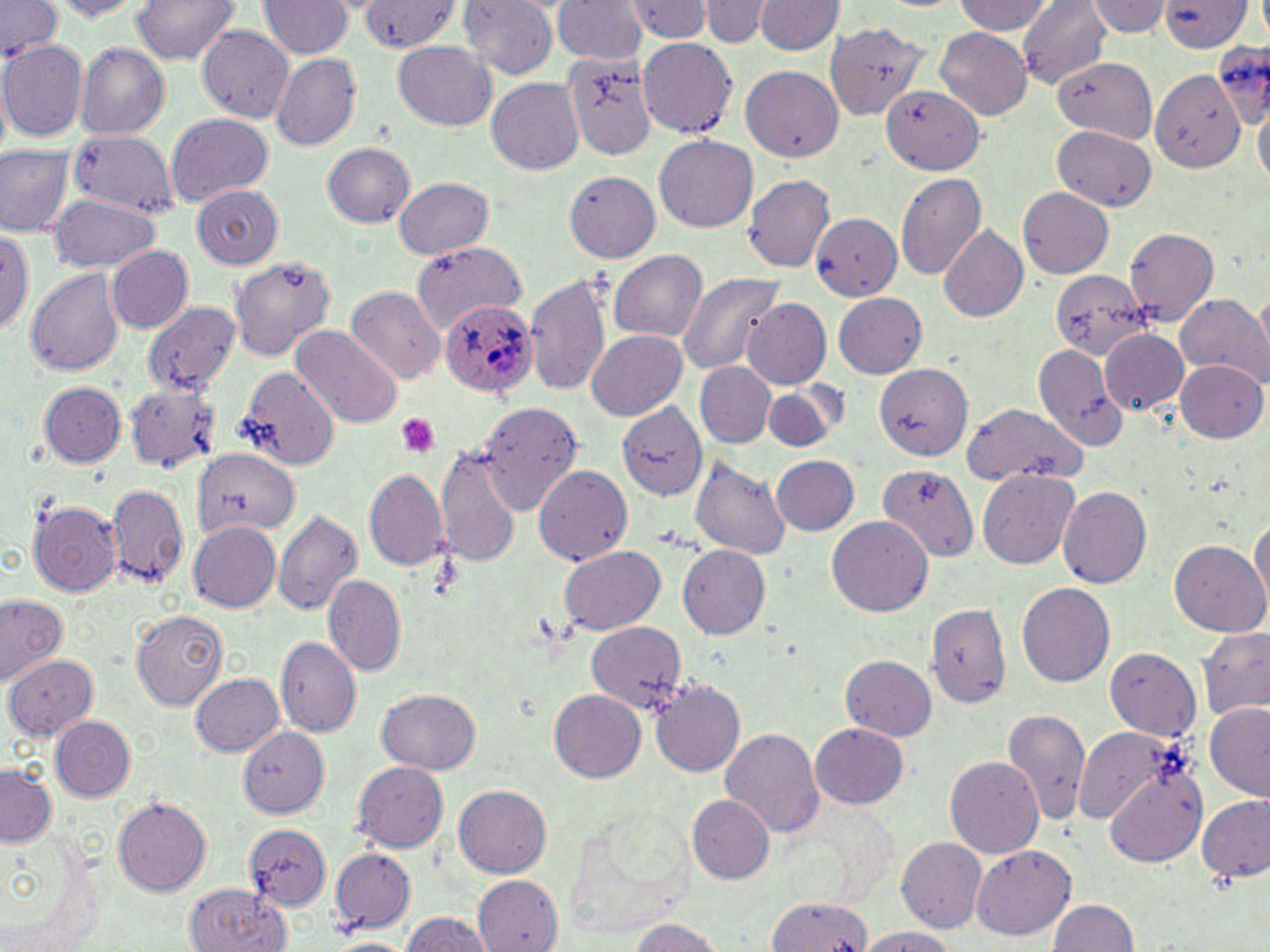
Plasmodium ovale-infected red blood cell locations = approximate bounding boxes as named x1/y1/x2/y2 corners in pixels: (x1=438, y1=297, x2=535, y2=396)
slide-level diagnosis = Plasmodium ovale
image size = 1270×952 pixels
platelet locations = approximate bounding boxes as named x1/y1/x2/y2 corners in pixels: (x1=396, y1=413, x2=439, y2=458)
field of view = one of a larger specimen
magnification = 1000x
stain = May-Grünwald-Giemsa
modality = optical microscopy
uninfected red blood cell locations = approximate bounding boxes as named x1/y1/x2/y2 corners in pixels: (x1=1, y1=0, x2=62, y2=57), (x1=129, y1=0, x2=240, y2=63), (x1=624, y1=0, x2=716, y2=44), (x1=695, y1=0, x2=777, y2=48), (x1=752, y1=0, x2=844, y2=56), (x1=1017, y1=0, x2=1111, y2=88), (x1=1086, y1=0, x2=1172, y2=37), (x1=45, y1=1, x2=154, y2=21), (x1=258, y1=1, x2=354, y2=59), (x1=359, y1=1, x2=459, y2=52), (x1=457, y1=1, x2=561, y2=78), (x1=551, y1=1, x2=648, y2=63), (x1=953, y1=1, x2=1051, y2=35), (x1=1160, y1=1, x2=1254, y2=51), (x1=823, y1=23, x2=931, y2=122), (x1=197, y1=24, x2=294, y2=121), (x1=935, y1=28, x2=1032, y2=117), (x1=636, y1=37, x2=739, y2=140), (x1=0, y1=39, x2=87, y2=141), (x1=1212, y1=39, x2=1270, y2=130), (x1=394, y1=41, x2=496, y2=131), (x1=75, y1=43, x2=169, y2=139), (x1=564, y1=51, x2=659, y2=161), (x1=270, y1=53, x2=361, y2=150), (x1=1054, y1=59, x2=1155, y2=139), (x1=742, y1=65, x2=842, y2=162), (x1=1150, y1=69, x2=1244, y2=173), (x1=486, y1=78, x2=583, y2=175), (x1=882, y1=85, x2=986, y2=175), (x1=1254, y1=101, x2=1269, y2=191), (x1=166, y1=111, x2=274, y2=205), (x1=1054, y1=128, x2=1156, y2=211), (x1=65, y1=129, x2=179, y2=219), (x1=653, y1=135, x2=757, y2=233), (x1=0, y1=144, x2=75, y2=236), (x1=322, y1=144, x2=415, y2=226), (x1=564, y1=169, x2=662, y2=261), (x1=896, y1=172, x2=987, y2=279), (x1=742, y1=174, x2=835, y2=271), (x1=393, y1=177, x2=493, y2=258), (x1=191, y1=184, x2=283, y2=269), (x1=1018, y1=186, x2=1114, y2=278), (x1=48, y1=194, x2=161, y2=272), (x1=810, y1=213, x2=902, y2=300), (x1=937, y1=224, x2=1029, y2=321), (x1=0, y1=227, x2=33, y2=335), (x1=1122, y1=227, x2=1218, y2=325), (x1=410, y1=241, x2=524, y2=329), (x1=106, y1=247, x2=193, y2=332), (x1=610, y1=249, x2=708, y2=342), (x1=229, y1=253, x2=336, y2=359), (x1=26, y1=268, x2=123, y2=377), (x1=1049, y1=269, x2=1148, y2=359), (x1=524, y1=271, x2=611, y2=396), (x1=676, y1=273, x2=783, y2=374), (x1=346, y1=285, x2=445, y2=384), (x1=1253, y1=291, x2=1270, y2=370), (x1=833, y1=293, x2=925, y2=377), (x1=1177, y1=294, x2=1269, y2=384), (x1=742, y1=298, x2=831, y2=388), (x1=142, y1=301, x2=243, y2=395), (x1=289, y1=323, x2=402, y2=428), (x1=587, y1=329, x2=687, y2=420), (x1=1101, y1=329, x2=1188, y2=413), (x1=1032, y1=343, x2=1130, y2=452), (x1=1175, y1=359, x2=1267, y2=442), (x1=695, y1=362, x2=776, y2=448), (x1=874, y1=365, x2=975, y2=460), (x1=238, y1=367, x2=339, y2=470), (x1=39, y1=381, x2=126, y2=466), (x1=121, y1=381, x2=223, y2=474), (x1=761, y1=382, x2=845, y2=453), (x1=477, y1=402, x2=582, y2=513), (x1=961, y1=402, x2=1086, y2=487), (x1=616, y1=403, x2=708, y2=502), (x1=191, y1=445, x2=299, y2=537), (x1=437, y1=447, x2=522, y2=568), (x1=771, y1=455, x2=858, y2=535), (x1=690, y1=456, x2=791, y2=559), (x1=878, y1=462, x2=981, y2=562), (x1=533, y1=465, x2=631, y2=564), (x1=976, y1=466, x2=1078, y2=568), (x1=363, y1=467, x2=450, y2=571), (x1=104, y1=482, x2=189, y2=588), (x1=1056, y1=485, x2=1151, y2=587), (x1=27, y1=500, x2=124, y2=596), (x1=272, y1=509, x2=362, y2=616), (x1=1250, y1=512, x2=1270, y2=610), (x1=827, y1=516, x2=932, y2=616), (x1=187, y1=520, x2=281, y2=612), (x1=1169, y1=540, x2=1268, y2=637), (x1=678, y1=545, x2=769, y2=638), (x1=558, y1=546, x2=667, y2=636), (x1=323, y1=574, x2=406, y2=675), (x1=1017, y1=583, x2=1115, y2=688), (x1=0, y1=592, x2=67, y2=686), (x1=926, y1=602, x2=1012, y2=710), (x1=131, y1=609, x2=229, y2=710), (x1=585, y1=621, x2=686, y2=713), (x1=1199, y1=628, x2=1270, y2=722), (x1=276, y1=635, x2=362, y2=736), (x1=1104, y1=646, x2=1202, y2=740), (x1=840, y1=654, x2=936, y2=740), (x1=5, y1=655, x2=99, y2=740), (x1=190, y1=673, x2=282, y2=755), (x1=648, y1=679, x2=746, y2=775), (x1=378, y1=689, x2=480, y2=773), (x1=550, y1=689, x2=644, y2=781), (x1=1204, y1=702, x2=1270, y2=802), (x1=1003, y1=706, x2=1087, y2=826), (x1=50, y1=716, x2=134, y2=800), (x1=809, y1=723, x2=909, y2=809), (x1=1074, y1=725, x2=1177, y2=827), (x1=238, y1=727, x2=330, y2=817), (x1=722, y1=728, x2=825, y2=836), (x1=945, y1=754, x2=1043, y2=859), (x1=354, y1=761, x2=448, y2=852), (x1=0, y1=763, x2=56, y2=848), (x1=1104, y1=767, x2=1205, y2=867), (x1=454, y1=784, x2=551, y2=878), (x1=688, y1=795, x2=775, y2=884), (x1=1198, y1=795, x2=1270, y2=881), (x1=112, y1=796, x2=212, y2=897), (x1=5, y1=823, x2=99, y2=952), (x1=245, y1=824, x2=330, y2=908), (x1=897, y1=837, x2=987, y2=932), (x1=969, y1=845, x2=1076, y2=942), (x1=329, y1=846, x2=414, y2=931), (x1=473, y1=874, x2=561, y2=951), (x1=184, y1=884, x2=290, y2=952), (x1=766, y1=896, x2=872, y2=950), (x1=1046, y1=899, x2=1139, y2=952), (x1=400, y1=911, x2=494, y2=952), (x1=627, y1=917, x2=726, y2=951), (x1=855, y1=926, x2=959, y2=952)
preparation = thin blood smear